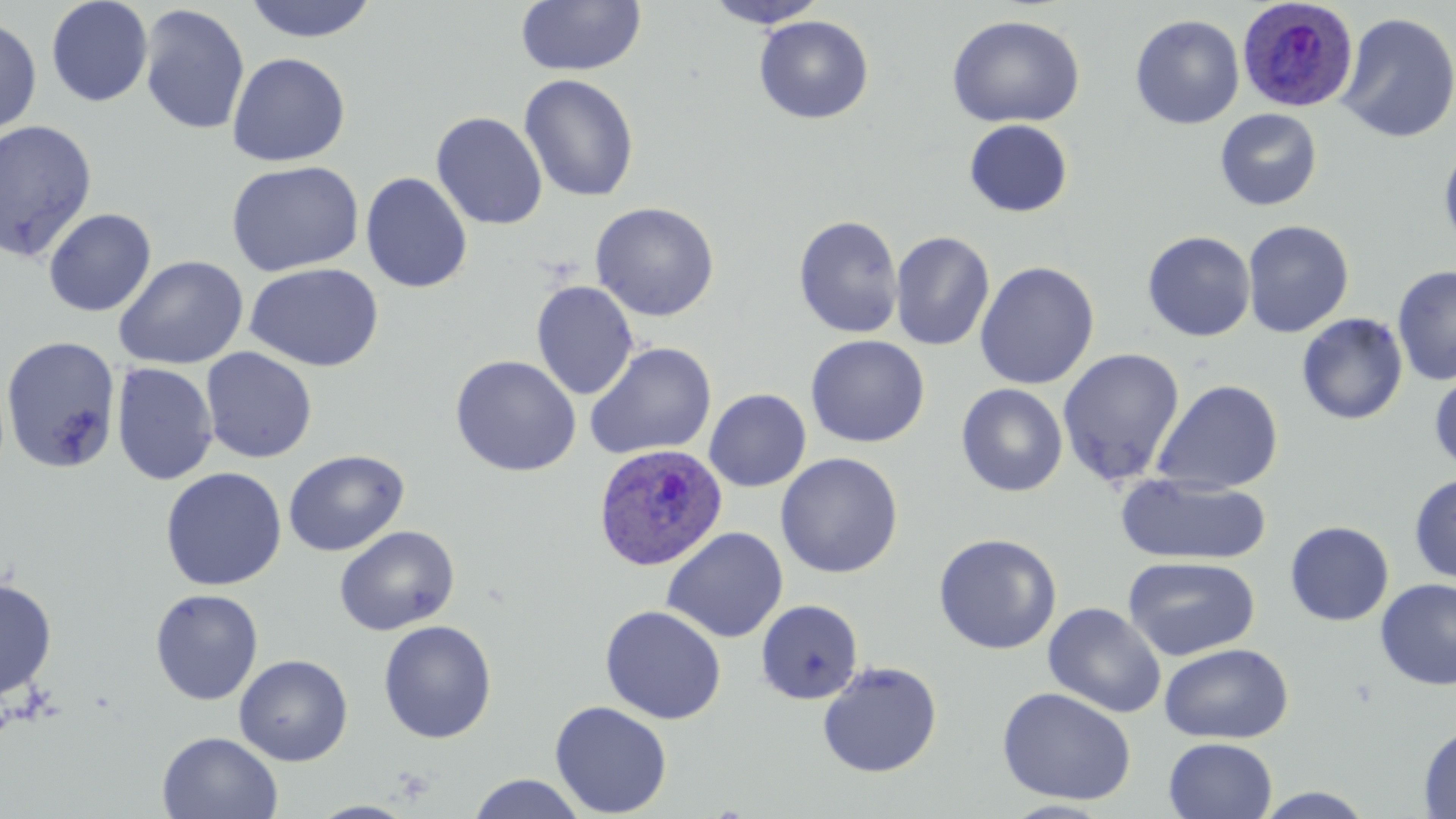

Approximate bounding boxes as [x1, y1, x2, y2] in pixels. Uninfected red blood cell locations: [45, 0, 153, 107], [242, 0, 379, 43], [515, 0, 647, 77], [706, 0, 828, 29], [138, 4, 251, 135], [1335, 12, 1456, 144], [946, 14, 1085, 128], [1130, 14, 1245, 129], [754, 15, 874, 124], [0, 16, 42, 136], [227, 51, 350, 167], [519, 73, 639, 203], [1214, 107, 1323, 211], [430, 111, 548, 230], [0, 119, 98, 262], [963, 119, 1074, 217], [1438, 142, 1456, 254], [225, 160, 364, 277], [360, 171, 473, 294], [590, 201, 720, 322], [43, 207, 156, 317], [793, 215, 904, 339], [1242, 220, 1355, 338], [890, 231, 995, 351], [1142, 231, 1256, 342], [114, 254, 248, 370], [974, 261, 1100, 390], [245, 262, 383, 372], [1392, 264, 1456, 386], [531, 280, 639, 400], [1296, 312, 1409, 426], [1, 335, 121, 474], [805, 335, 930, 448], [584, 342, 717, 461], [201, 347, 317, 463], [1057, 348, 1186, 487], [450, 354, 582, 477], [111, 361, 219, 486], [1429, 368, 1456, 476], [1150, 379, 1284, 494], [955, 383, 1068, 497], [704, 388, 811, 492], [283, 449, 408, 556], [775, 452, 903, 579], [160, 467, 288, 591], [1115, 473, 1273, 566], [1409, 473, 1456, 584], [1285, 521, 1394, 626], [334, 525, 460, 636], [661, 527, 788, 643], [932, 532, 1062, 655], [1123, 556, 1260, 661], [0, 576, 58, 701], [1374, 578, 1456, 691], [150, 588, 264, 705], [756, 599, 864, 705], [1043, 601, 1167, 718], [600, 605, 726, 724], [378, 620, 497, 744], [1159, 643, 1294, 744], [234, 654, 353, 766], [817, 661, 943, 778], [997, 686, 1138, 806], [549, 700, 673, 817], [1418, 723, 1456, 817], [157, 731, 283, 819], [1163, 737, 1278, 819], [468, 773, 586, 819], [1253, 787, 1377, 818], [1001, 799, 1117, 818], [306, 801, 420, 818]. Plasmodium ovale-infected red blood cell locations: [1236, 0, 1359, 112], [592, 443, 728, 572]. Slide-level diagnosis: Plasmodium ovale. Single field of view. Captured at 1000x magnification. Thin blood film. May-Grünwald-Giemsa-stained preparation. Image is 1456×819 pixels. Light microscopy.